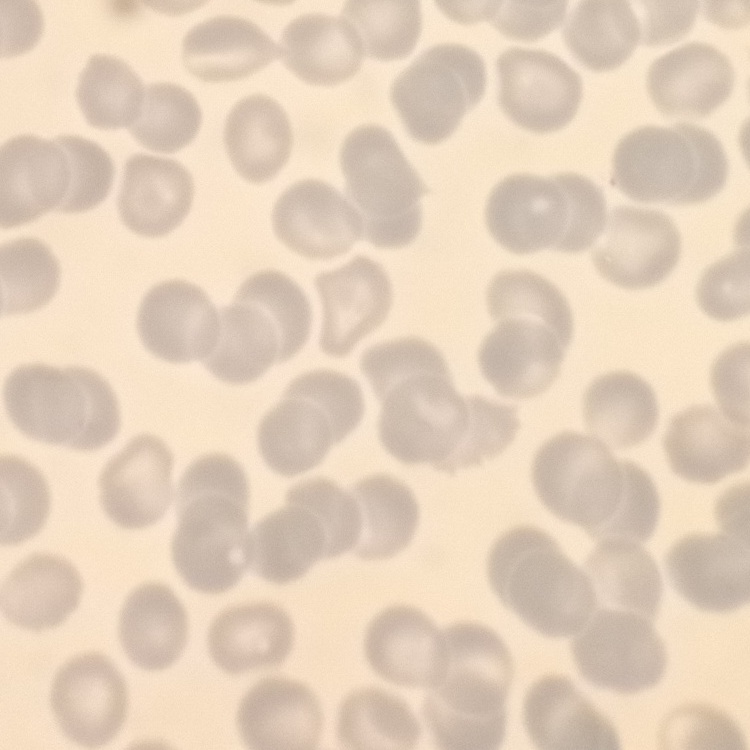
erythrocyte morphology = no rouleaux formation
image type = square crop of a larger photomicrograph
stain = Field's or Giemsa
preparation = thin blood film